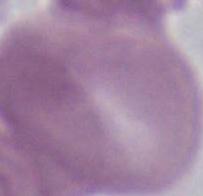

magnification = 1000x
identification = erythrocyte
modality = photomicrograph